Assess this cell for malaria.
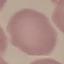
It is uninfected.

Giemsa stain. Thin blood smear. Cell patch, automatically extracted from a larger field of view and resized to 64 × 64 pixels. Photographed with a smartphone camera at the microscope eyepiece.